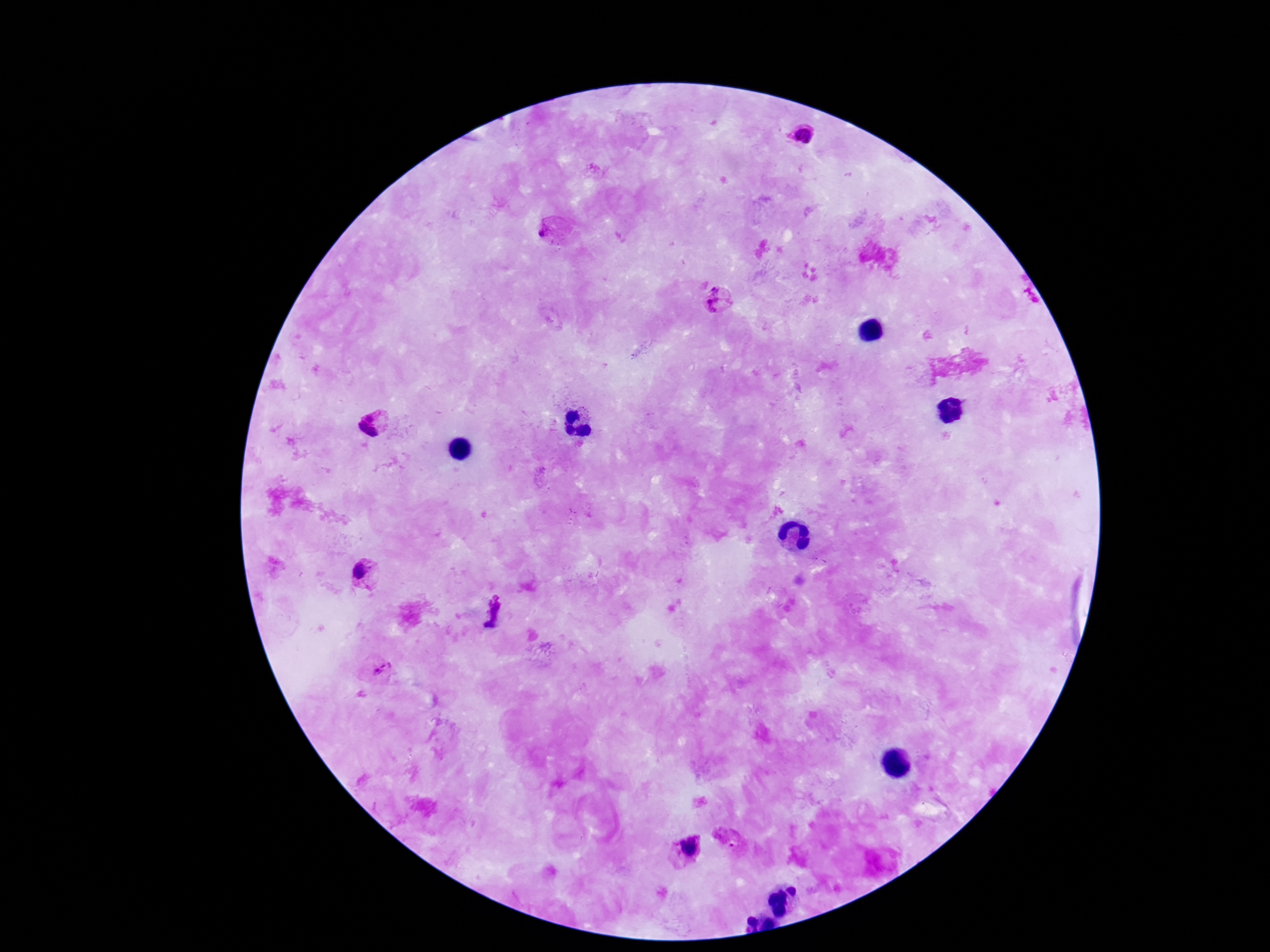
field_of_view: one from this slide
patient_malaria_status: infected
plasmodium_parasite_locations: 'approximate centers as [x, y] in pixels: [803, 136], [543, 232], [717, 297], [371, 416], [362, 425], [371, 432], [359, 572], [496, 609], [490, 626], [383, 669], [727, 838], [689, 847]'
magnification: 100x
image_size: 1270×952 pixels
stain: Giemsa
capture: smartphone camera through the microscope eyepiece
preparation: thick blood smear